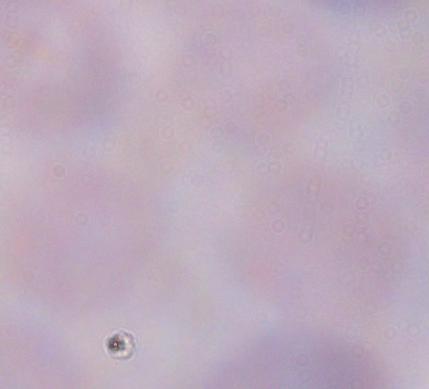
Summary:
  - Magnification: 1000x
  - Modality: micrograph
  - Identification: trypanosome